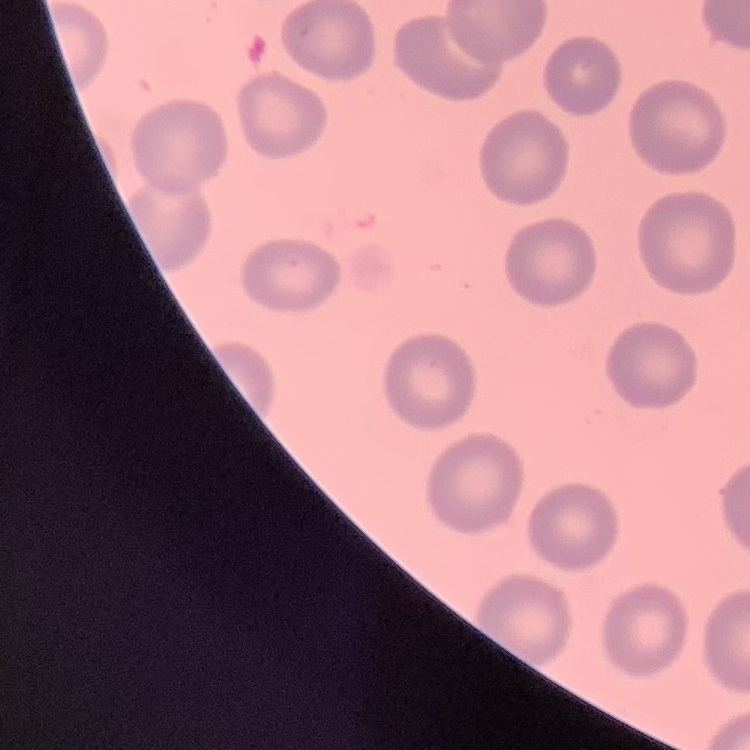

Summary:
  - Erythrocyte morphology: no rouleaux formation
  - Stain: Field's or Giemsa
  - Image type: one tile cut from a larger photomicrograph
  - Preparation: thin blood smear